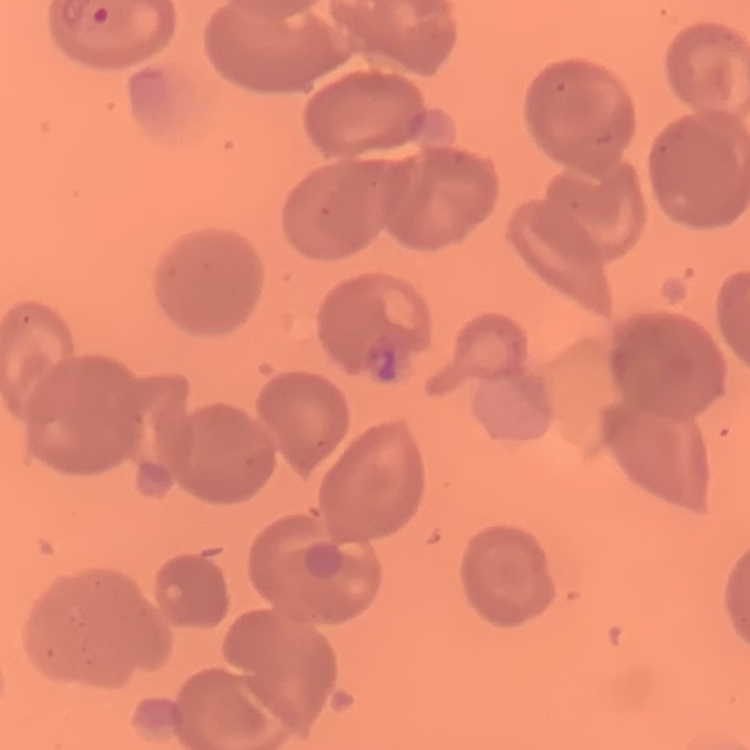
{
  "erythrocyte_morphology": "no rouleaux formation",
  "image_type": "square crop of a larger photomicrograph",
  "stain": "Field's or Giemsa",
  "preparation": "thin peripheral smear"
}